Name the parasite shown.
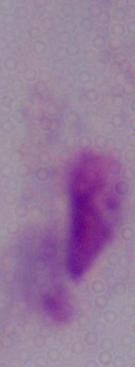
This is a trichomonad.

Micrograph. Captured at 1000x magnification.